Locate every malaria parasite.
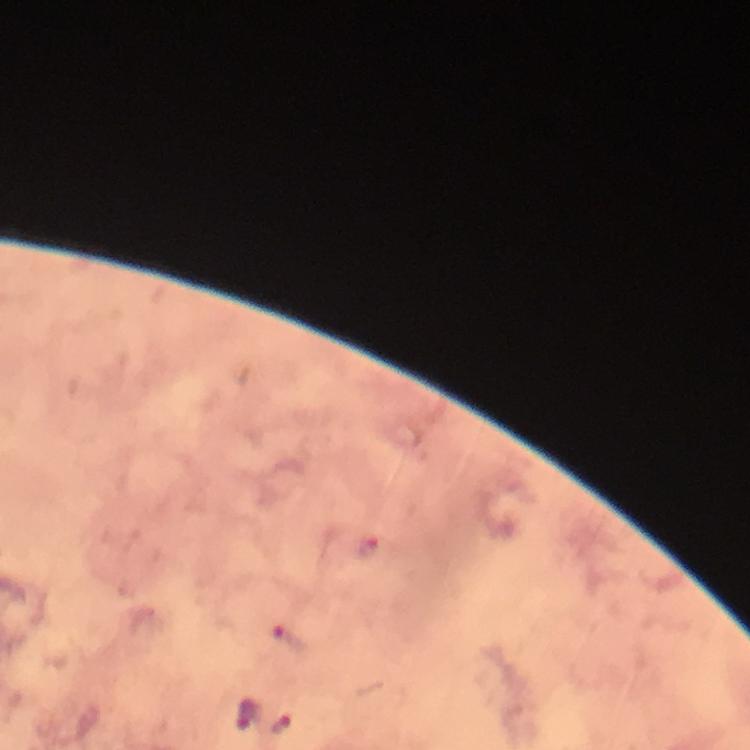
Approximate object centers, in pixels from the top-left corner.
Malaria parasites: (x=370, y=544), (x=288, y=636), (x=247, y=712), (x=281, y=725).

Summary:
  - Magnification: 100x
  - Immersion oil: used
  - Capture: smartphone photograph through a microscope
  - Image size: 750×750 pixels
  - Preparation: thick smear
  - Context: from a diagnostic examination for malaria
  - Cropped from: one field of view
  - Stain: Giemsa